Name the parasite shown.
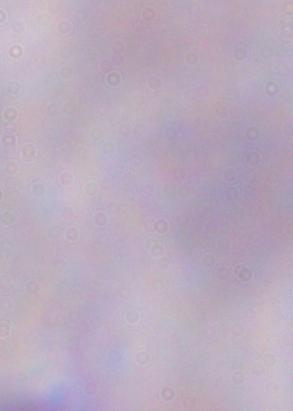
A trypanosome.

Summary:
  - Magnification: 1000x
  - Modality: photomicrograph